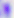 Toxoplasma gondii is shown. Photomicrograph. Captured at 400x magnification.